Classify this cell by malaria status.
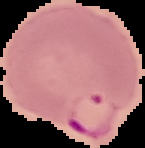

It is parasitized.

Image is 145×148 pixels. Segmented cell region on a black background. From a thin blood film.